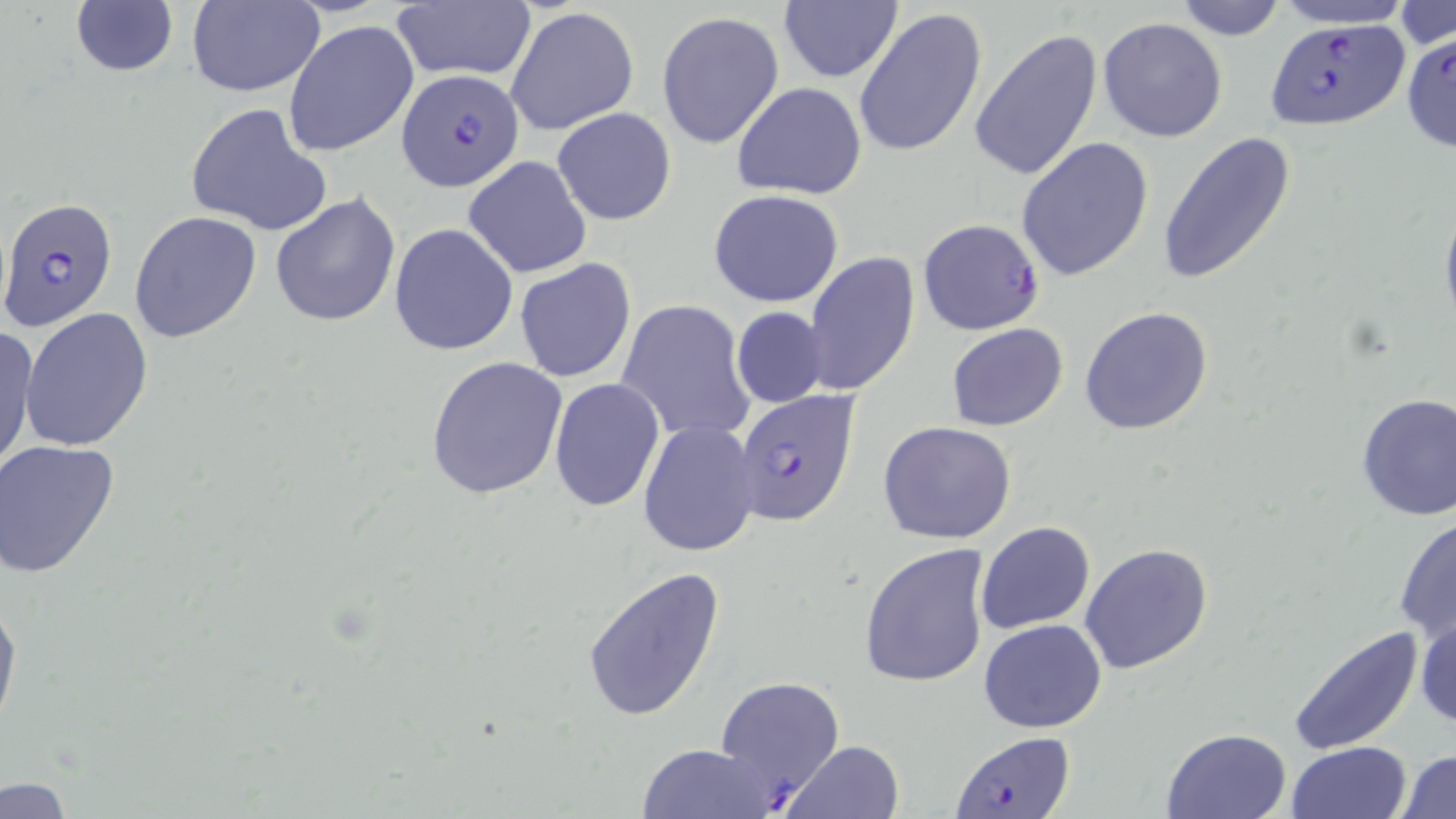

slide-level diagnosis = Plasmodium falciparum
stain = May-Grünwald-Giemsa
magnification = 1000x
uninfected red blood cell locations = approximate bounding boxes as named x1/y1/x2/y2 corners in pixels: (x1=186, y1=0, x2=326, y2=97), (x1=388, y1=0, x2=538, y2=84), (x1=777, y1=0, x2=902, y2=85), (x1=1170, y1=0, x2=1292, y2=39), (x1=1268, y1=0, x2=1417, y2=30), (x1=68, y1=2, x2=181, y2=80), (x1=1393, y1=3, x2=1455, y2=51), (x1=506, y1=6, x2=639, y2=137), (x1=853, y1=9, x2=988, y2=160), (x1=657, y1=10, x2=785, y2=149), (x1=1098, y1=16, x2=1227, y2=142), (x1=284, y1=21, x2=420, y2=157), (x1=969, y1=29, x2=1102, y2=184), (x1=732, y1=83, x2=867, y2=200), (x1=185, y1=102, x2=333, y2=236), (x1=552, y1=107, x2=677, y2=226), (x1=1158, y1=132, x2=1296, y2=287), (x1=1015, y1=137, x2=1153, y2=281), (x1=464, y1=155, x2=592, y2=278), (x1=708, y1=190, x2=846, y2=308), (x1=269, y1=191, x2=401, y2=327), (x1=1440, y1=197, x2=1456, y2=334), (x1=129, y1=210, x2=261, y2=343), (x1=389, y1=223, x2=519, y2=357), (x1=806, y1=253, x2=920, y2=398), (x1=514, y1=258, x2=637, y2=384), (x1=615, y1=299, x2=755, y2=446), (x1=731, y1=306, x2=830, y2=409), (x1=20, y1=308, x2=155, y2=452), (x1=1079, y1=308, x2=1213, y2=435), (x1=946, y1=323, x2=1069, y2=430), (x1=0, y1=325, x2=38, y2=475), (x1=424, y1=357, x2=567, y2=500), (x1=549, y1=378, x2=665, y2=512), (x1=1354, y1=391, x2=1456, y2=524), (x1=637, y1=419, x2=761, y2=558), (x1=877, y1=420, x2=1017, y2=544), (x1=0, y1=440, x2=122, y2=579), (x1=1393, y1=513, x2=1456, y2=648), (x1=974, y1=521, x2=1095, y2=636), (x1=858, y1=542, x2=992, y2=689), (x1=1079, y1=542, x2=1214, y2=674), (x1=580, y1=564, x2=728, y2=724), (x1=0, y1=591, x2=21, y2=736), (x1=1413, y1=611, x2=1456, y2=732), (x1=978, y1=620, x2=1107, y2=733), (x1=1288, y1=625, x2=1426, y2=755), (x1=1160, y1=728, x2=1290, y2=818), (x1=780, y1=739, x2=907, y2=819), (x1=1285, y1=741, x2=1414, y2=819), (x1=638, y1=743, x2=780, y2=819), (x1=1397, y1=747, x2=1456, y2=819), (x1=0, y1=779, x2=75, y2=817)
Plasmodium falciparum-infected red blood cell locations = approximate bounding boxes as named x1/y1/x2/y2 corners in pixels: (x1=1263, y1=20, x2=1409, y2=132), (x1=1401, y1=30, x2=1456, y2=154), (x1=396, y1=69, x2=522, y2=191), (x1=0, y1=196, x2=120, y2=331), (x1=918, y1=218, x2=1045, y2=336), (x1=731, y1=390, x2=862, y2=526), (x1=715, y1=674, x2=845, y2=809), (x1=952, y1=732, x2=1073, y2=818)
modality = optical microscopy
preparation = thin blood smear
image size = 1456×819 pixels
field of view = one of a larger specimen